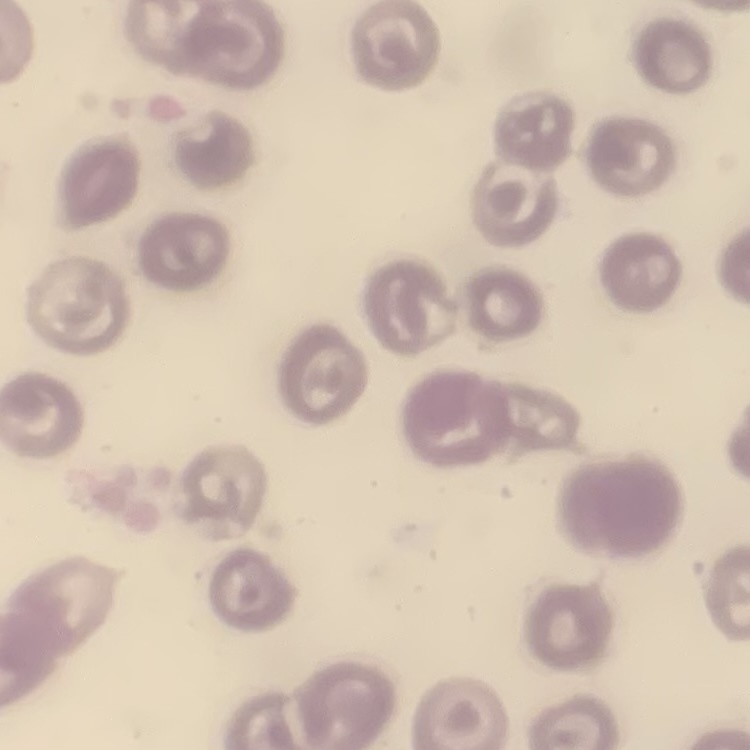

The red blood cells show no rouleaux formation. Thin blood film. Square crop of a larger photomicrograph. Stained with either Field's or Giemsa.